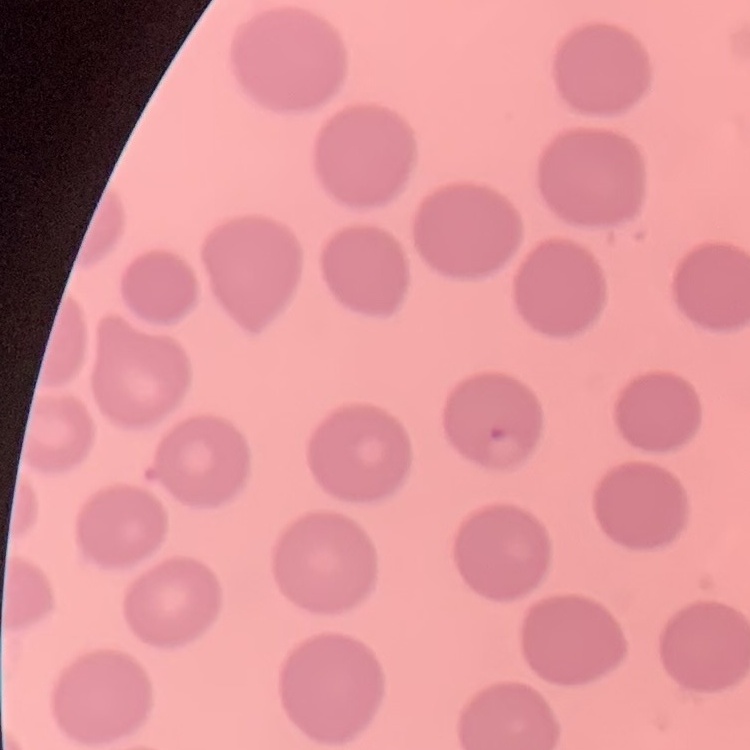
Summary:
  - Red blood cell morphology: no rouleaux formation
  - Preparation: thin peripheral smear
  - Stain: Field's or Giemsa
  - Image type: one tile cut from a larger photomicrograph